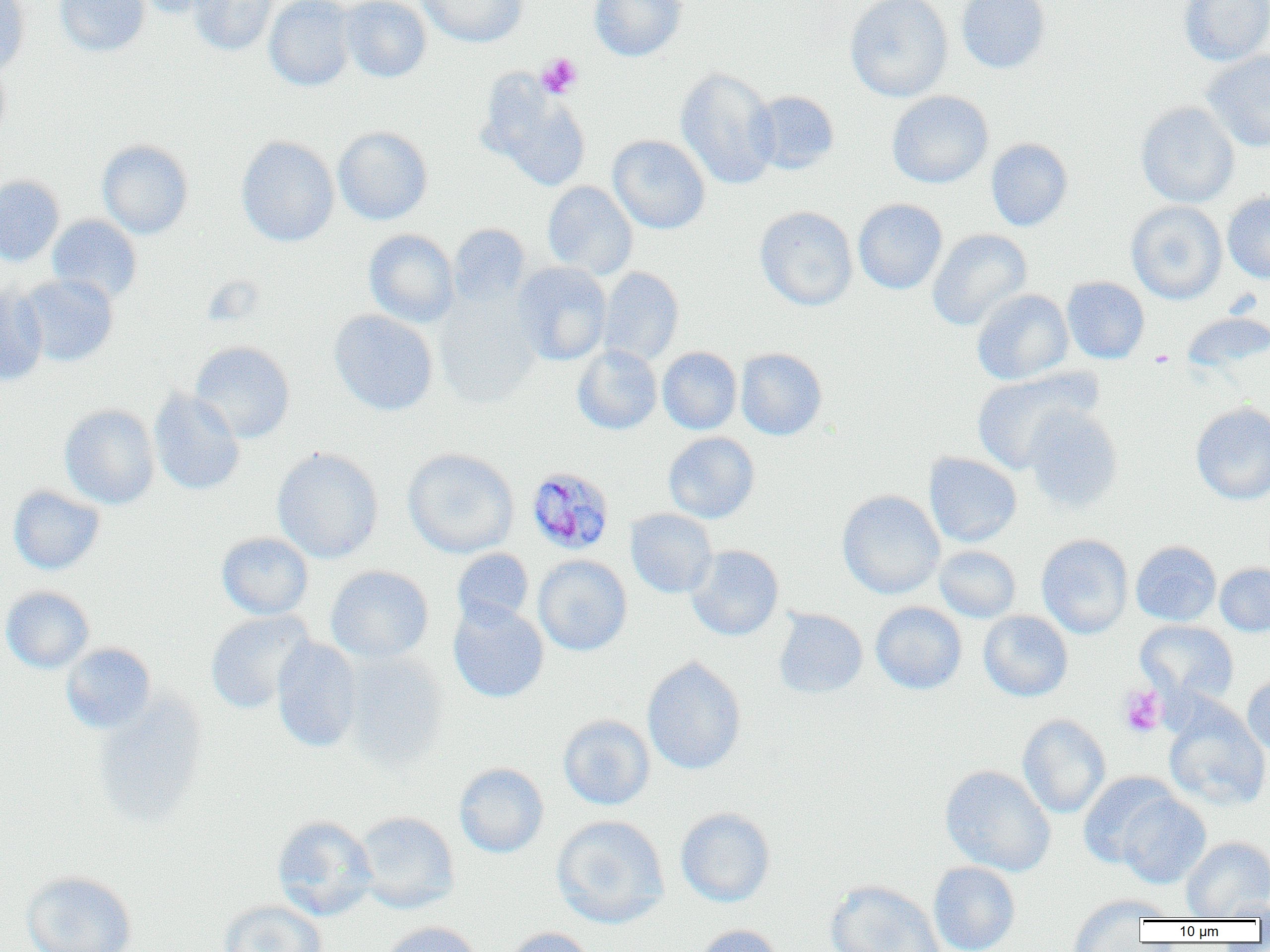

Approximate bounding boxes as (x1, y1, x2, y2) in pixels. Platelet locations: (536, 53, 583, 99), (1149, 350, 1176, 369), (1119, 684, 1167, 738). Plasmodium malariae-infected red blood cell locations: (526, 466, 616, 555). Uninfected red blood cell locations: (0, 0, 29, 74), (55, 0, 150, 56), (133, 0, 223, 19), (188, 0, 278, 56), (264, 0, 356, 91), (339, 0, 432, 83), (417, 0, 528, 47), (589, 0, 687, 62), (845, 0, 953, 102), (956, 0, 1051, 74), (1178, 0, 1270, 66), (1201, 50, 1270, 152), (0, 61, 10, 142), (675, 67, 780, 190), (477, 74, 592, 190), (749, 90, 840, 174), (886, 91, 994, 189), (1136, 102, 1239, 208), (333, 126, 433, 225), (236, 135, 340, 247), (607, 135, 710, 234), (986, 138, 1073, 231), (97, 140, 194, 239), (0, 174, 65, 266), (542, 181, 638, 280), (1222, 192, 1270, 283), (853, 198, 947, 294), (1126, 201, 1227, 305), (754, 206, 858, 310), (47, 214, 142, 305), (448, 224, 530, 307), (363, 229, 460, 327), (927, 229, 1032, 330), (512, 262, 612, 365), (598, 267, 684, 366), (17, 274, 119, 367), (1062, 277, 1150, 364), (0, 285, 48, 385), (972, 289, 1073, 385), (433, 295, 541, 409), (329, 310, 438, 416), (1181, 312, 1269, 372), (190, 341, 295, 443), (572, 344, 662, 435), (657, 347, 742, 434), (736, 348, 827, 440), (971, 369, 1096, 474), (148, 388, 245, 496), (1190, 402, 1270, 505), (59, 403, 160, 509), (1023, 404, 1123, 512), (663, 432, 760, 523), (272, 447, 384, 564), (402, 447, 519, 558), (923, 452, 1022, 547), (8, 485, 106, 575), (836, 490, 945, 599), (625, 509, 717, 598), (216, 532, 314, 619), (1036, 534, 1133, 639), (1131, 541, 1221, 626), (686, 545, 784, 641), (934, 546, 1020, 623), (452, 548, 534, 629), (449, 550, 618, 635), (533, 555, 632, 656), (1215, 562, 1270, 636), (325, 565, 434, 663), (1, 586, 94, 673), (448, 601, 549, 703), (870, 601, 967, 694), (772, 608, 868, 698), (205, 610, 314, 714), (978, 610, 1073, 702), (1135, 619, 1239, 706), (272, 637, 363, 753), (60, 642, 157, 734), (342, 651, 449, 773), (642, 657, 746, 775), (1242, 673, 1270, 757), (91, 692, 208, 831), (1162, 700, 1270, 813), (558, 714, 655, 810), (1017, 714, 1111, 818), (454, 763, 549, 858), (939, 764, 1057, 877), (1078, 772, 1180, 869), (1115, 791, 1211, 889), (675, 807, 776, 907), (355, 811, 460, 913), (272, 815, 378, 921), (551, 815, 670, 929), (1181, 836, 1270, 919), (928, 861, 1021, 952), (20, 871, 138, 952), (824, 880, 945, 952), (1066, 894, 1167, 950), (1215, 897, 1270, 920), (218, 899, 328, 952), (378, 921, 484, 952), (693, 924, 785, 952), (500, 926, 596, 952). Slide-level diagnosis: Plasmodium malariae. Captured at 1000x magnification. Single field of view. Thin blood smear. Optical microscopy. Image is 1270×952 pixels.